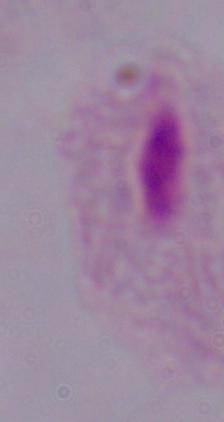
Summary:
  - Magnification: 1000x
  - Identification: trichomonad
  - Modality: photomicrograph